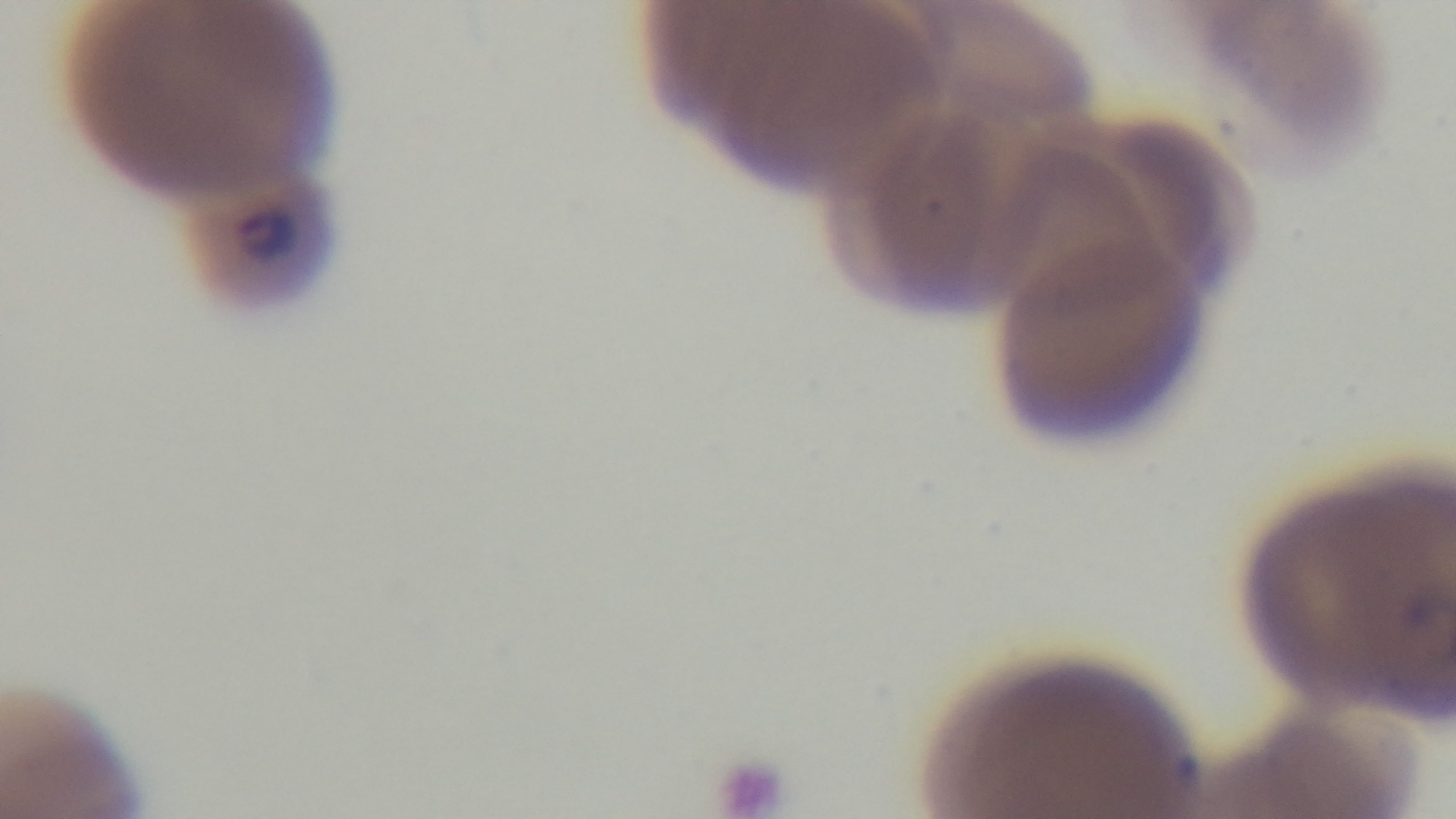

capture = mounted 4K digital camera
objective = 100x oil immersion
modality = light microscopy
field of view = one from the slide
malaria status = positive
preparation = thin smear
stain = Giemsa